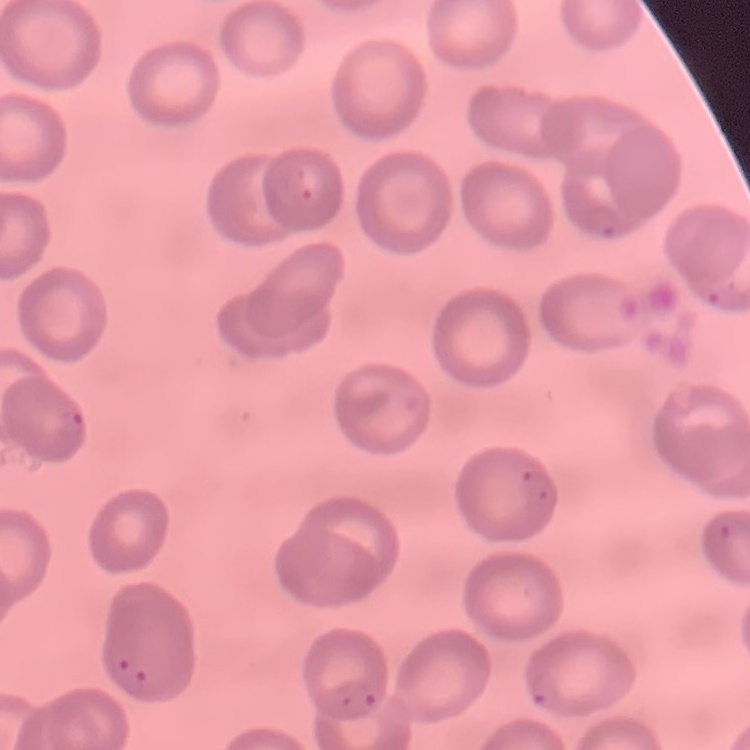

The red blood cells exhibit no rouleaux formation. Thin blood smear. Field's or Giemsa stain. Square crop of a larger photomicrograph.